Report the malaria status of this cell.
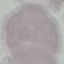
Uninfected.

preparation = thin smear
capture = smartphone through the microscope eyepiece
stain = Giemsa
image type = automatically extracted cell patch, resized to 64 × 64 pixels